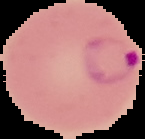
Summary:
  - Preparation: thin blood smear
  - Image type: segmented cell region with the area outside set to black
  - Image size: 145×139 pixels
  - Malaria status: parasitized